Identify the parasite.
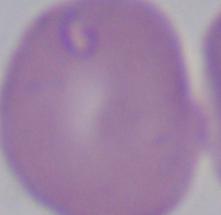
This is Babesia.

{
  "modality": "photomicrograph",
  "magnification": "1000x"
}